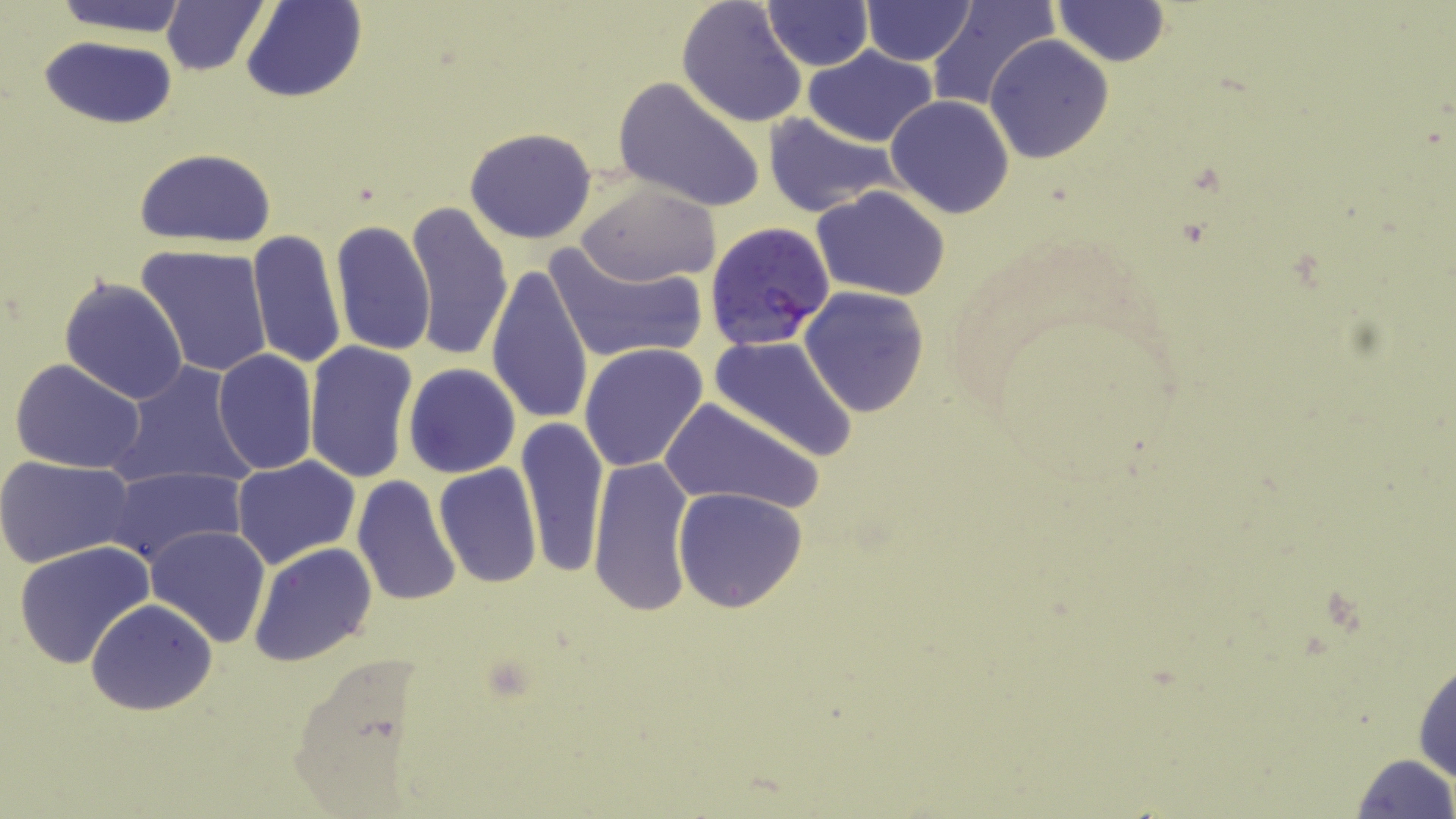

slide-level diagnosis = Plasmodium falciparum
stain = May-Grünwald-Giemsa
image size = 1456×819 pixels
Plasmodium falciparum-infected red blood cell locations = approximate bounding boxes as named x1/y1/x2/y2 corners in pixels: (x1=705, y1=221, x2=836, y2=352)
uninfected red blood cell locations = approximate bounding boxes as named x1/y1/x2/y2 corners in pixels: (x1=48, y1=0, x2=193, y2=37), (x1=161, y1=0, x2=269, y2=75), (x1=242, y1=0, x2=365, y2=103), (x1=677, y1=0, x2=809, y2=128), (x1=859, y1=0, x2=978, y2=67), (x1=925, y1=0, x2=1057, y2=112), (x1=1053, y1=0, x2=1169, y2=66), (x1=759, y1=1, x2=873, y2=70), (x1=38, y1=35, x2=179, y2=128), (x1=985, y1=35, x2=1114, y2=163), (x1=802, y1=46, x2=941, y2=148), (x1=612, y1=75, x2=767, y2=213), (x1=884, y1=94, x2=1016, y2=220), (x1=762, y1=111, x2=907, y2=219), (x1=464, y1=127, x2=597, y2=244), (x1=133, y1=148, x2=278, y2=248), (x1=574, y1=181, x2=720, y2=287), (x1=812, y1=185, x2=952, y2=299), (x1=406, y1=201, x2=513, y2=361), (x1=330, y1=220, x2=437, y2=359), (x1=247, y1=229, x2=346, y2=371), (x1=543, y1=240, x2=705, y2=366), (x1=137, y1=244, x2=274, y2=377), (x1=485, y1=262, x2=593, y2=428), (x1=60, y1=276, x2=188, y2=405), (x1=799, y1=286, x2=929, y2=416), (x1=708, y1=335, x2=859, y2=462), (x1=303, y1=341, x2=418, y2=485), (x1=579, y1=343, x2=709, y2=472), (x1=211, y1=350, x2=319, y2=475), (x1=9, y1=358, x2=149, y2=474), (x1=111, y1=361, x2=256, y2=491), (x1=403, y1=363, x2=520, y2=478), (x1=659, y1=398, x2=822, y2=515), (x1=516, y1=416, x2=609, y2=580), (x1=231, y1=456, x2=360, y2=571), (x1=588, y1=456, x2=695, y2=618), (x1=0, y1=457, x2=135, y2=567), (x1=432, y1=462, x2=542, y2=587), (x1=105, y1=466, x2=246, y2=568), (x1=352, y1=475, x2=463, y2=609), (x1=673, y1=487, x2=807, y2=613), (x1=145, y1=524, x2=271, y2=647), (x1=11, y1=540, x2=155, y2=667), (x1=249, y1=542, x2=377, y2=668), (x1=86, y1=599, x2=217, y2=715), (x1=1412, y1=648, x2=1456, y2=789), (x1=1348, y1=753, x2=1454, y2=819)
modality = light microscopy
preparation = thin blood film
magnification = 1000x
field of view = one of a larger specimen